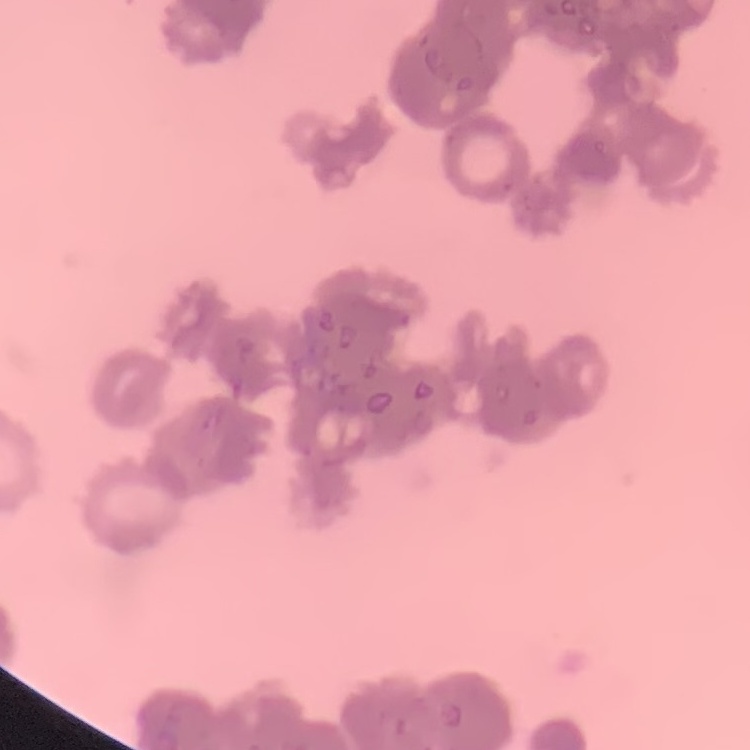
Summary:
  - Red blood cell morphology: rouleaux formation
  - Stain: Field's or Giemsa
  - Preparation: thin peripheral smear
  - Image type: square crop of a larger photomicrograph